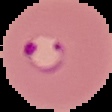

Summary:
  - Malaria status: parasitized
  - Image type: segmented cell region on a black background
  - Preparation: thin blood smear
  - Image size: 112×112 pixels